Classify this cell by malaria status.
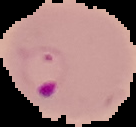
Parasitized.

Summary:
  - Image type: segmented cell region on a black background
  - Image size: 136×127 pixels
  - Preparation: thin blood smear